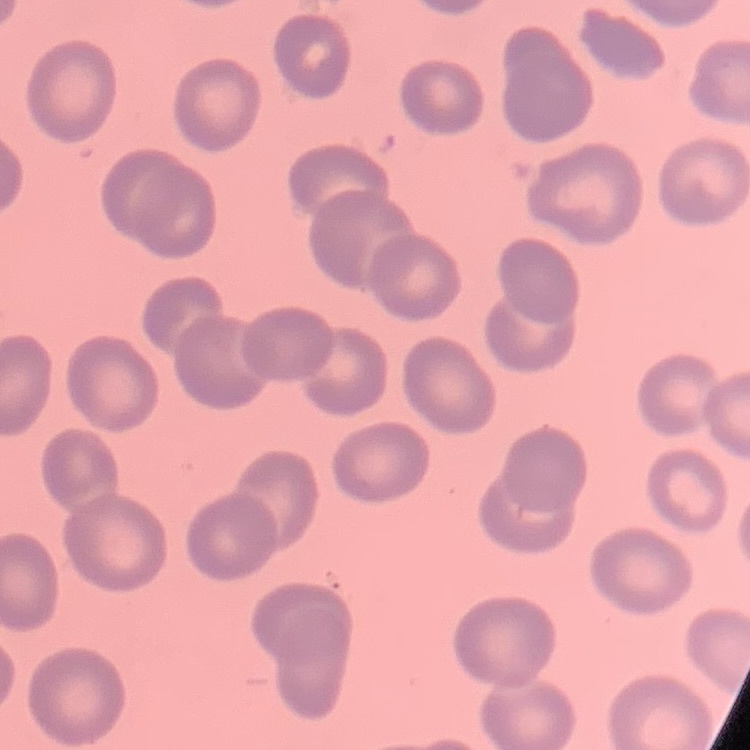

{
  "red_blood_cell_morphology": "no rouleaux formation",
  "image_type": "one tile cut from a larger photomicrograph",
  "stain": "Field's or Giemsa",
  "preparation": "thin peripheral smear"
}